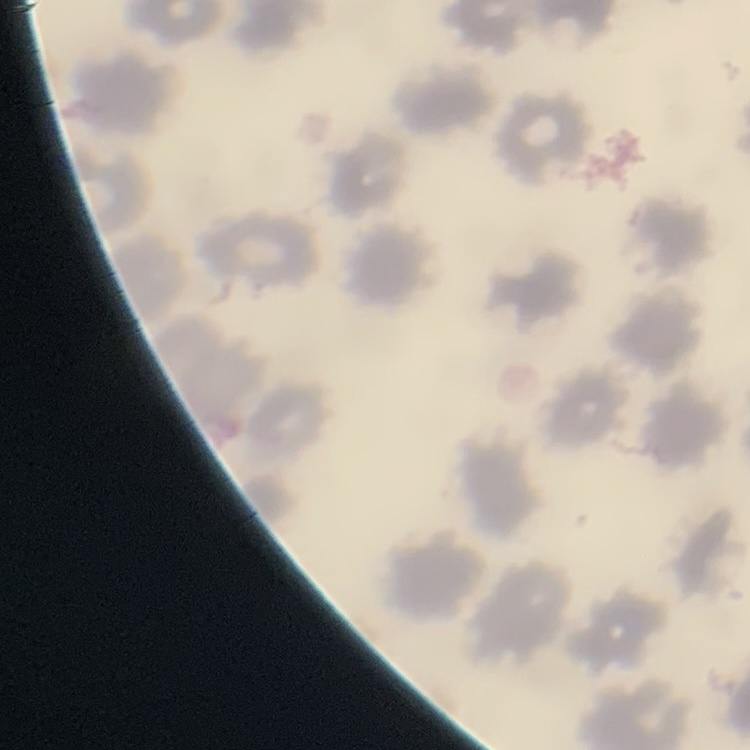
Summary:
  - Erythrocyte morphology: no rouleaux formation
  - Image type: one tile cut from a larger photomicrograph
  - Preparation: thin blood smear
  - Stain: Field's or Giemsa